Give the position of every malaria parasite.
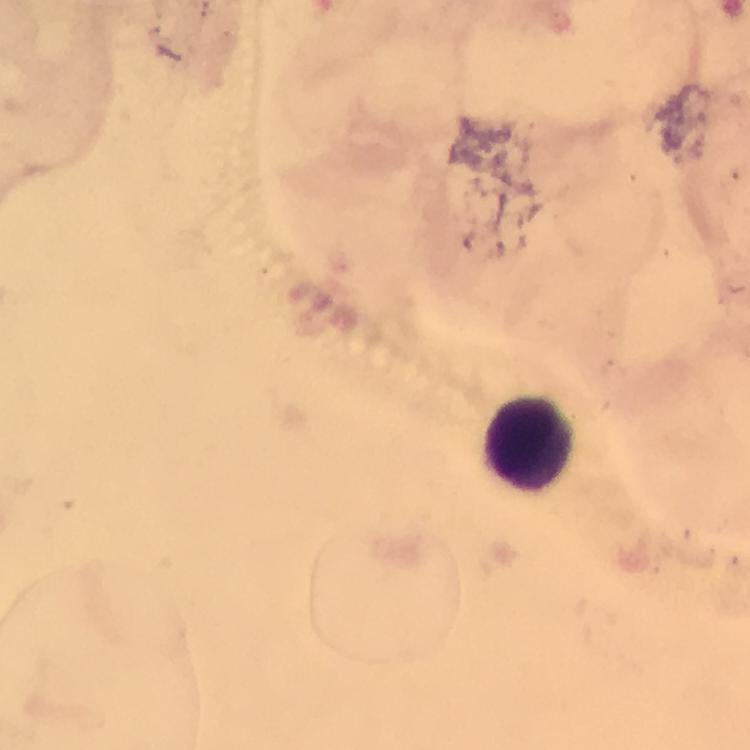
No malaria parasites seen.

Approximate centers as [x, y] in pixels. Leukocyte locations: [530, 440]. From a diagnostic examination for malaria. Giemsa-stained preparation. A crop from one field of view. Thick blood smear. Immersion oil applied. Photographed with a smartphone mounted on the microscope. 100x magnification. Image is 750×750 pixels.